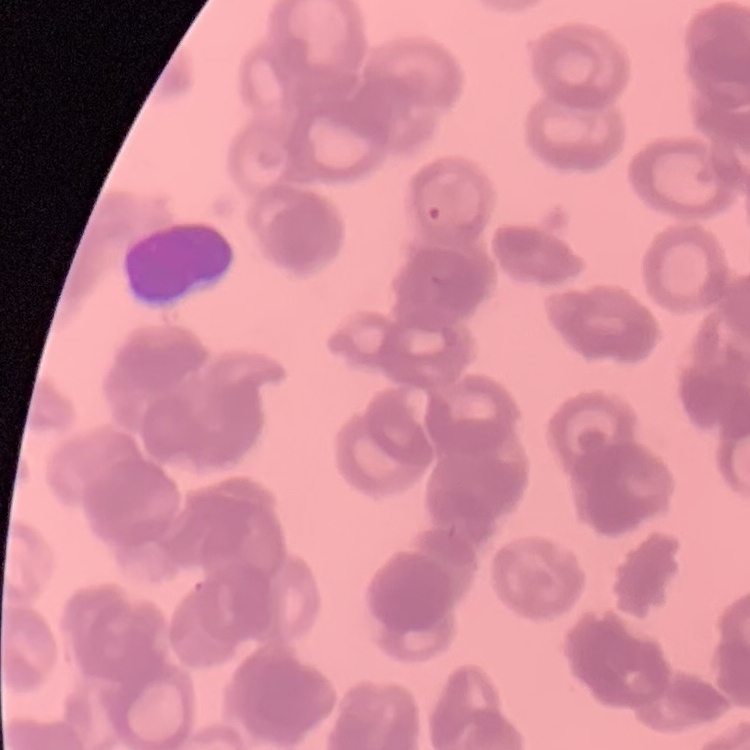 The red blood cells show rouleaux formation. Stained with either Field's or Giemsa. Thin blood smear. Square crop of a larger photomicrograph.